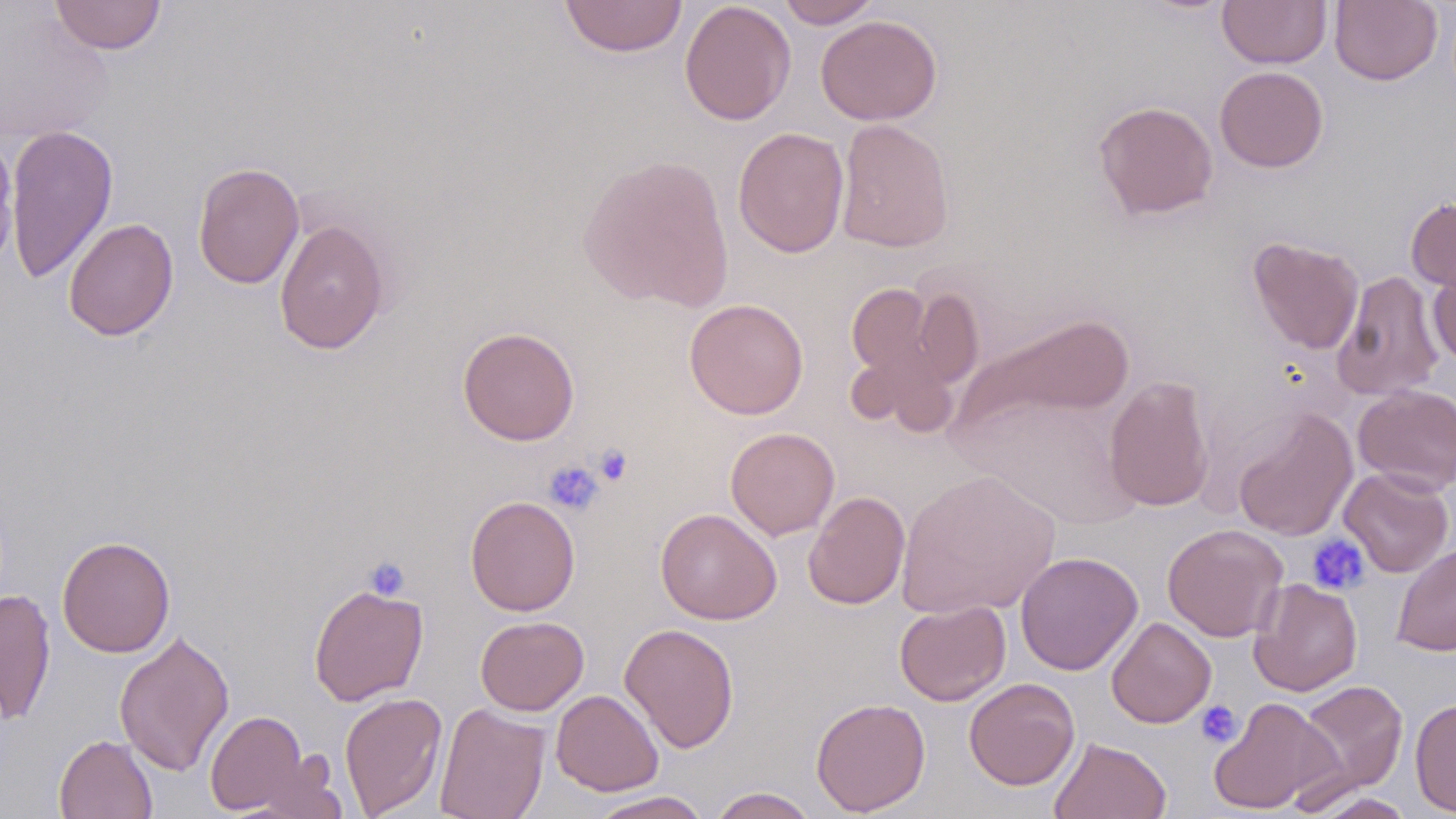

Approximate bounding boxes as named x1/y1/x2/y2 corners in pixels. Uninfected red blood cell locations: (x1=49, y1=0, x2=167, y2=55), (x1=558, y1=0, x2=688, y2=58), (x1=776, y1=0, x2=882, y2=29), (x1=1217, y1=0, x2=1331, y2=68), (x1=1330, y1=0, x2=1442, y2=86), (x1=679, y1=1, x2=796, y2=126), (x1=815, y1=15, x2=942, y2=125), (x1=1214, y1=66, x2=1328, y2=172), (x1=1093, y1=100, x2=1218, y2=220), (x1=835, y1=118, x2=955, y2=253), (x1=4, y1=124, x2=119, y2=284), (x1=732, y1=126, x2=850, y2=258), (x1=577, y1=153, x2=735, y2=311), (x1=192, y1=162, x2=305, y2=289), (x1=1406, y1=196, x2=1456, y2=294), (x1=63, y1=218, x2=179, y2=341), (x1=274, y1=219, x2=391, y2=355), (x1=1248, y1=237, x2=1364, y2=354), (x1=1428, y1=258, x2=1456, y2=367), (x1=1332, y1=269, x2=1445, y2=401), (x1=845, y1=282, x2=942, y2=385), (x1=911, y1=286, x2=984, y2=389), (x1=683, y1=298, x2=809, y2=419), (x1=965, y1=313, x2=1135, y2=431), (x1=457, y1=326, x2=580, y2=446), (x1=846, y1=346, x2=960, y2=437), (x1=1103, y1=375, x2=1215, y2=512), (x1=1353, y1=383, x2=1456, y2=494), (x1=952, y1=391, x2=1145, y2=532), (x1=1232, y1=407, x2=1358, y2=542), (x1=725, y1=427, x2=840, y2=539), (x1=1339, y1=467, x2=1454, y2=577), (x1=896, y1=468, x2=1061, y2=619), (x1=803, y1=491, x2=910, y2=609), (x1=464, y1=496, x2=580, y2=616), (x1=655, y1=508, x2=781, y2=625), (x1=1162, y1=523, x2=1288, y2=642), (x1=57, y1=535, x2=176, y2=658), (x1=1392, y1=543, x2=1456, y2=656), (x1=1015, y1=551, x2=1143, y2=675), (x1=1249, y1=578, x2=1363, y2=697), (x1=308, y1=582, x2=429, y2=706), (x1=0, y1=589, x2=56, y2=724), (x1=894, y1=600, x2=1011, y2=706), (x1=475, y1=615, x2=589, y2=716), (x1=1106, y1=616, x2=1216, y2=728), (x1=620, y1=623, x2=740, y2=753), (x1=114, y1=630, x2=235, y2=775), (x1=964, y1=677, x2=1080, y2=790), (x1=1295, y1=680, x2=1408, y2=799), (x1=551, y1=689, x2=664, y2=796), (x1=339, y1=692, x2=448, y2=818), (x1=1207, y1=696, x2=1341, y2=814), (x1=810, y1=697, x2=931, y2=816), (x1=1410, y1=698, x2=1456, y2=817), (x1=434, y1=703, x2=551, y2=819), (x1=204, y1=709, x2=314, y2=816), (x1=54, y1=734, x2=158, y2=819), (x1=1048, y1=736, x2=1171, y2=818), (x1=708, y1=787, x2=818, y2=818), (x1=585, y1=791, x2=715, y2=819), (x1=1306, y1=791, x2=1417, y2=818). Platelet locations: (x1=593, y1=443, x2=634, y2=487), (x1=543, y1=460, x2=604, y2=516), (x1=1307, y1=533, x2=1370, y2=595), (x1=363, y1=555, x2=411, y2=600), (x1=1195, y1=700, x2=1243, y2=748). Slide-level diagnosis: no evidence of blood parasites. May-Grünwald-Giemsa-stained preparation. Single field of view. Image is 1456×819 pixels. Thin blood film. Optical microscopy. 1000x magnification.